Name the cell type shown.
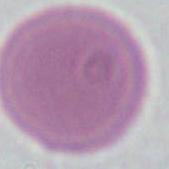
This is an erythrocyte.

Summary:
  - Modality: micrograph
  - Magnification: 1000x